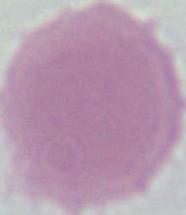 1000x magnification. A red blood cell is seen. Micrograph.